Locate and identify every blood parasite.
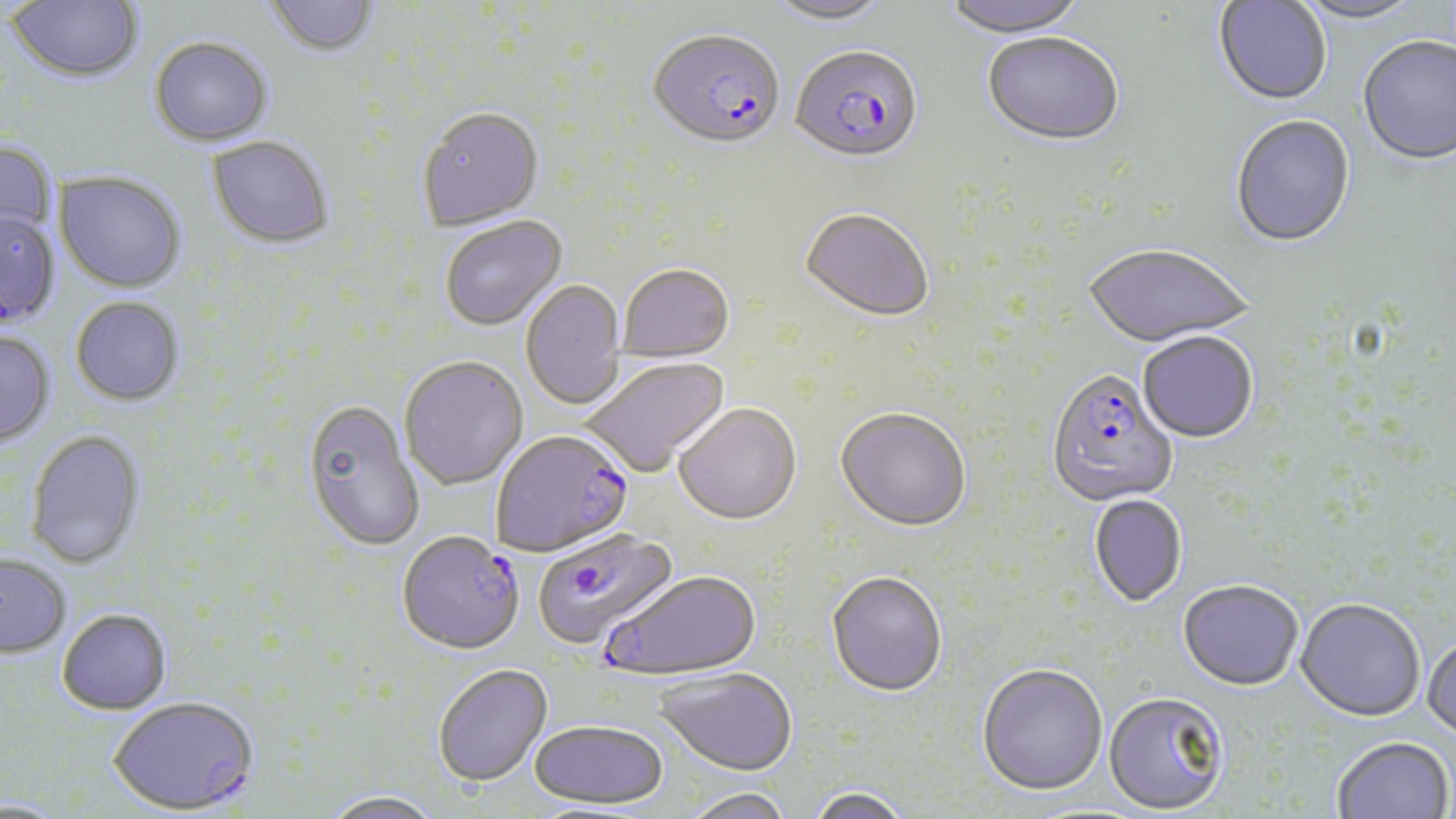

Approximate bounding boxes as (x1, y1, x2, y2) in pixels.
Plasmodium falciparum-infected red blood cells: (648, 33, 786, 154), (791, 48, 924, 167), (1047, 372, 1178, 508), (491, 432, 634, 560), (533, 528, 681, 654), (397, 535, 525, 657), (603, 571, 763, 684), (109, 700, 260, 817).
No Plasmodium ovale, Plasmodium malariae, Plasmodium vivax, Babesia divergens, or Trypanosoma brucei observed.

Uninfected red blood cell locations: (6, 0, 144, 84), (263, 0, 380, 60), (939, 0, 1090, 40), (1292, 0, 1428, 27), (765, 1, 894, 29), (1214, 1, 1332, 107), (982, 36, 1124, 149), (149, 38, 274, 148), (1357, 38, 1456, 168), (417, 110, 545, 233), (1231, 117, 1355, 250), (205, 137, 335, 252), (0, 139, 59, 250), (53, 172, 187, 294), (799, 211, 934, 324), (0, 212, 60, 329), (440, 217, 568, 334), (1083, 246, 1255, 350), (618, 266, 735, 365), (521, 280, 627, 410), (70, 298, 185, 409), (0, 332, 57, 449), (1138, 334, 1258, 445), (580, 357, 732, 479), (399, 358, 528, 492), (300, 402, 425, 553), (674, 406, 802, 528), (836, 411, 971, 534), (24, 430, 147, 571), (1089, 495, 1187, 608), (0, 556, 71, 660), (826, 573, 947, 699), (1178, 580, 1303, 691), (1295, 599, 1425, 723), (57, 611, 172, 717), (1423, 635, 1456, 741), (977, 665, 1108, 798), (434, 666, 553, 789), (653, 670, 797, 779), (1103, 693, 1230, 816), (529, 724, 668, 812), (1334, 737, 1453, 819), (806, 788, 912, 819), (681, 789, 794, 819), (320, 793, 445, 819). Slide-level diagnosis: Plasmodium falciparum. 1000x magnification. Single field of view. May-Grünwald-Giemsa-stained preparation. Optical microscopy. Thin blood smear. Image is 1456×819 pixels.